Assess this cell for malaria.
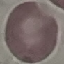
It is uninfected.

Summary:
  - Capture: smartphone camera at the microscope eyepiece
  - Stain: Giemsa
  - Image type: cell patch, automatically extracted from a larger field of view and resized to 64 × 64 pixels
  - Preparation: thin blood film